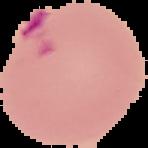

Summary:
  - Image type: segmented cell region with the area outside set to black
  - Preparation: thin blood smear
  - Result: Plasmodium parasites identified
  - Image size: 148×148 pixels